Identify the parasite.
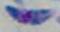
Toxoplasma gondii.

Micrograph. 1000x magnification.